State which cell type is depicted.
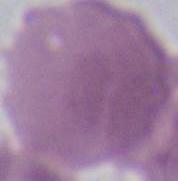
This is an erythrocyte.

Photomicrograph. 1000x magnification.